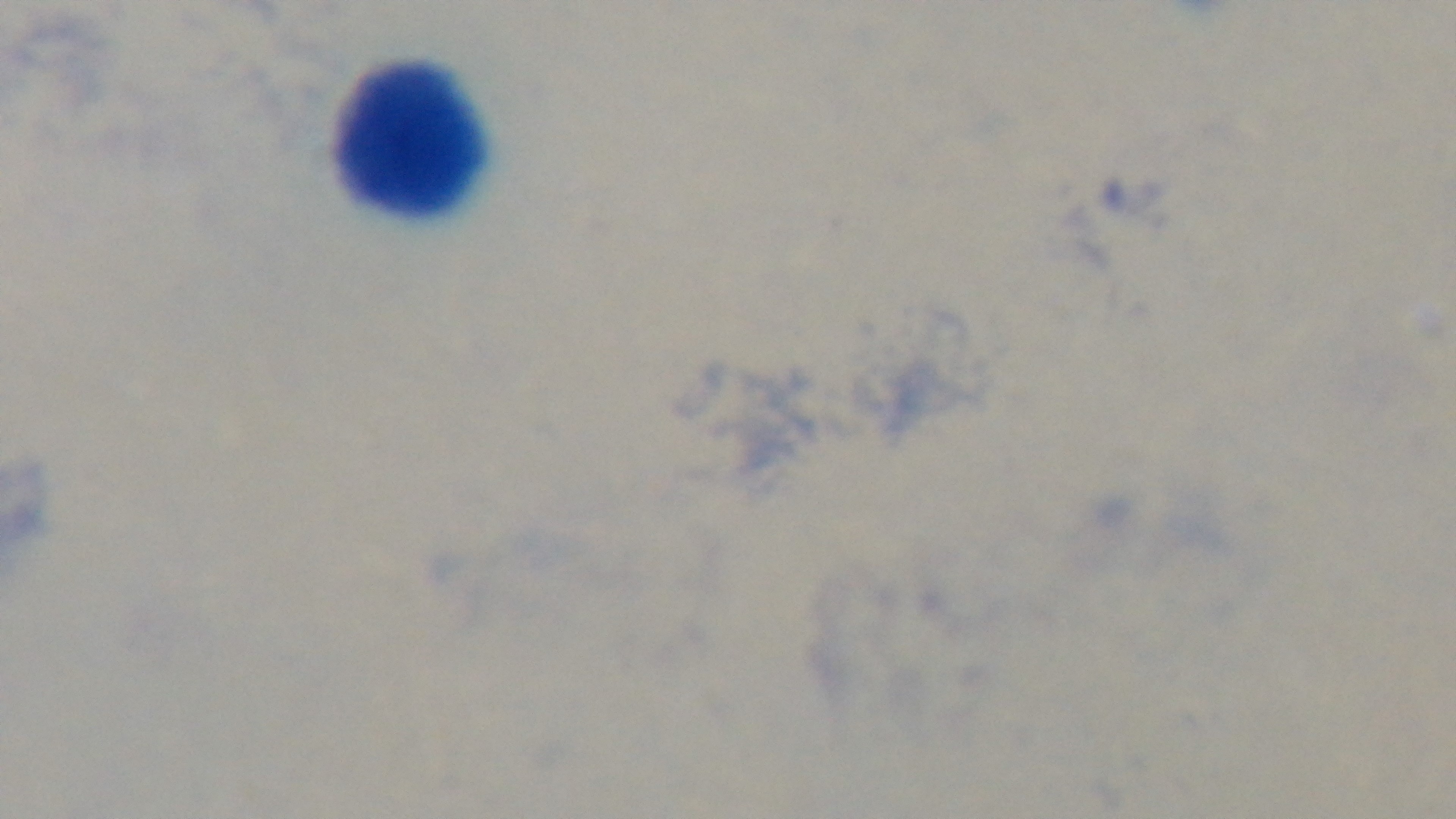
Summary:
  - Malaria status: negative
  - Modality: light microscopy
  - Stain: Giemsa
  - Objective: 100x oil immersion
  - Field of view: one from the slide
  - Capture: mounted 4K digital camera
  - Preparation: thick smear